Name the parasite shown.
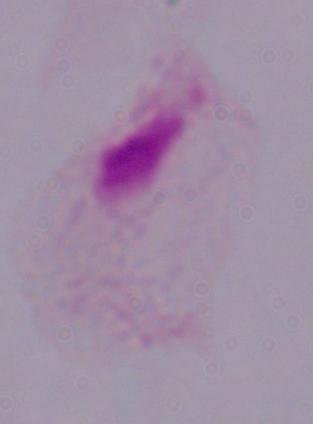

A trichomonad.

Captured at 1000x magnification. Micrograph.